Report the malaria status of this cell.
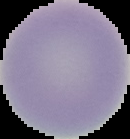
Uninfected.

Summary:
  - Image type: segmented cell region on a black background
  - Preparation: thin blood film
  - Image size: 130×139 pixels